Report the malaria status of this cell.
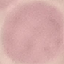
Uninfected.

Giemsa-stained preparation. Automatically extracted cell patch, resized to 64 × 64 pixels. Acquired by smartphone through the microscope eyepiece. Thin smear of blood.